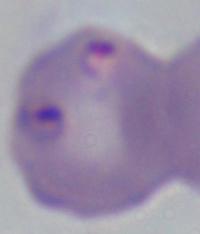

identification = Babesia
modality = photomicrograph
magnification = 1000x